Comment on the morphology of the red blood cells.
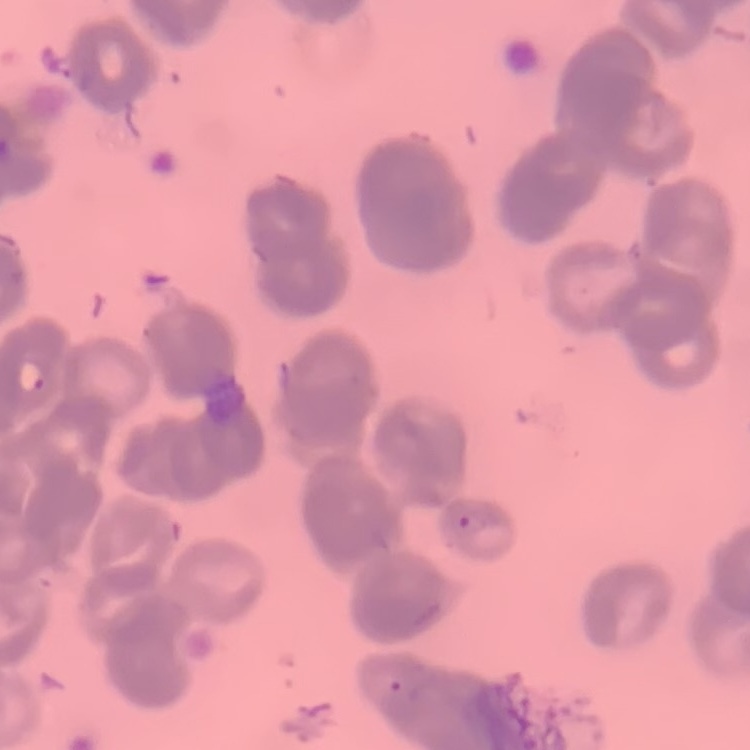
They show rouleaux formation.

Thin blood smear. Field's or Giemsa stain. Square crop of a larger photomicrograph.